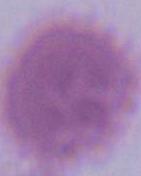

Micrograph. An erythrocyte is seen. Captured at 1000x magnification.